Give the position of every Plasmodium parasite visible.
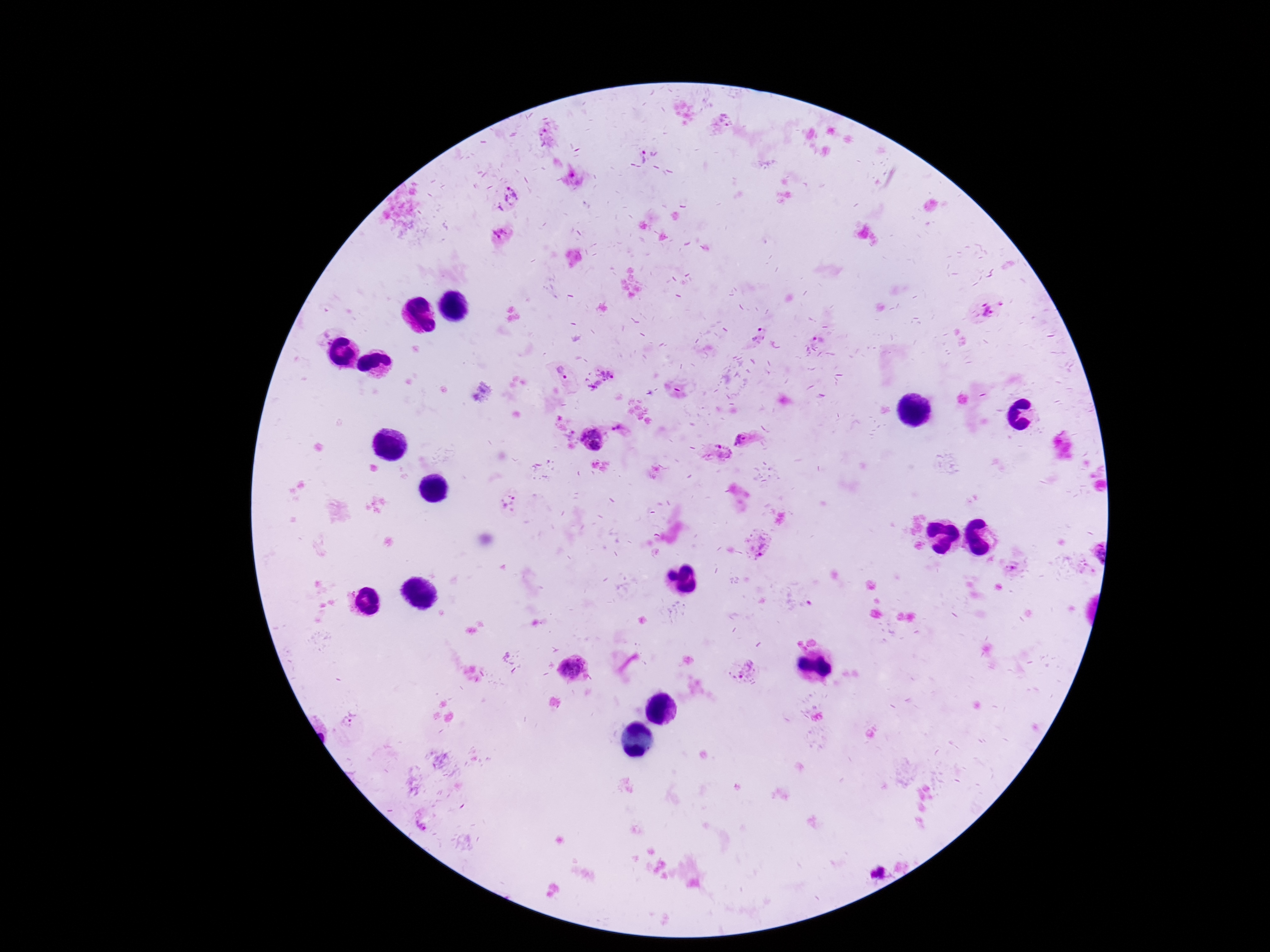

Approximate object centers, in pixels from the top-left corner.
Plasmodium parasites: (x=723, y=121), (x=642, y=154), (x=507, y=197), (x=500, y=236), (x=992, y=307), (x=758, y=332), (x=818, y=338), (x=562, y=372), (x=606, y=373), (x=620, y=430), (x=592, y=439), (x=744, y=440), (x=718, y=453), (x=759, y=544), (x=1012, y=564), (x=746, y=669), (x=575, y=670), (x=875, y=872).

Summary:
  - Field of view: single
  - Magnification: 100x
  - Preparation: thick peripheral-blood smear
  - Capture: smartphone camera through the microscope eyepiece
  - Patient malaria status: infected
  - Stain: Giemsa
  - Image size: 1270×952 pixels